Describe the morphology of the red blood cells.
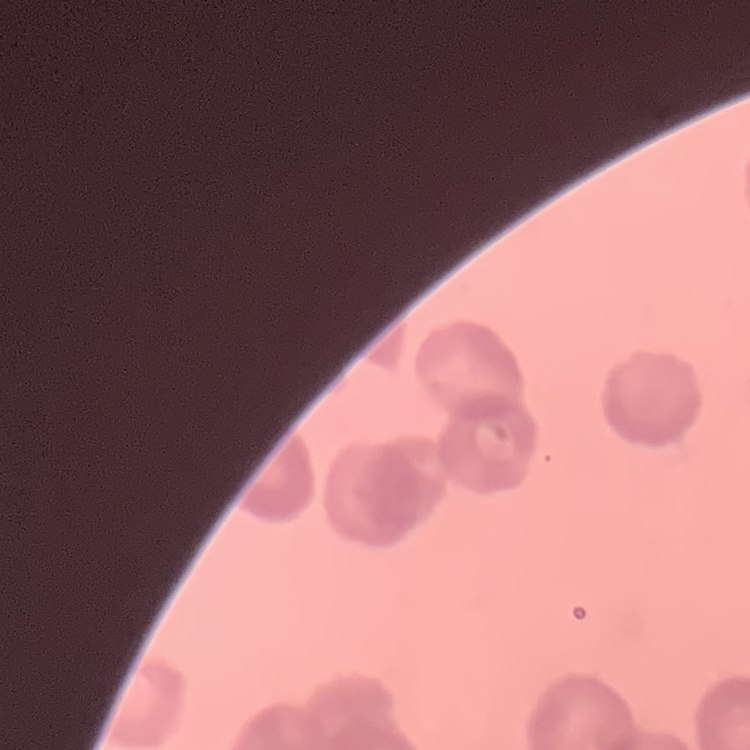
Rouleaux formation.

image type = one tile cut from a larger photomicrograph
stain = Field's or Giemsa
preparation = thin blood film